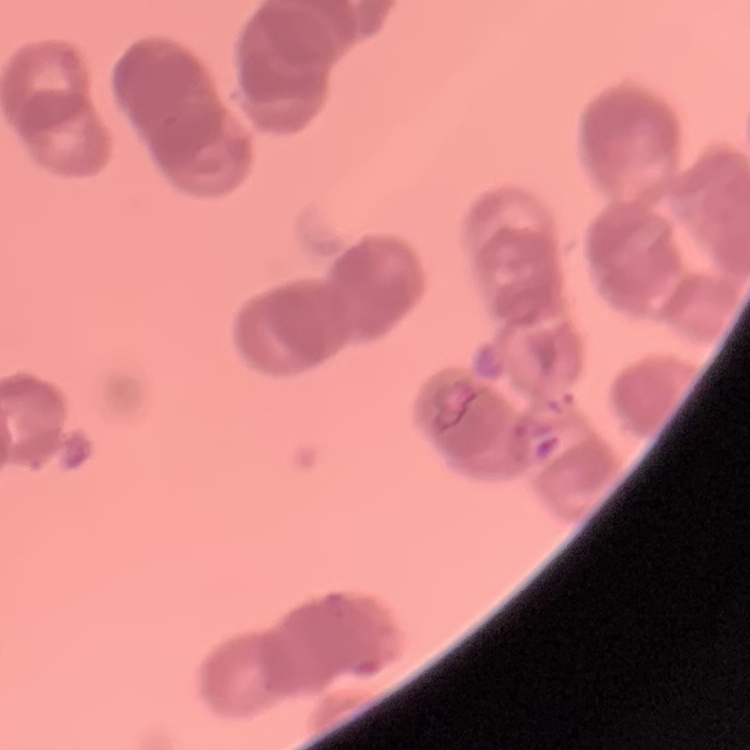
{
  "erythrocyte_morphology": "rouleaux formation",
  "preparation": "thin blood film",
  "stain": "Field's or Giemsa",
  "image_type": "square crop of a larger photomicrograph"
}